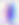
Captured at 400x magnification. Toxoplasma gondii is shown. Photomicrograph.